Comment on the morphology of the red blood cells.
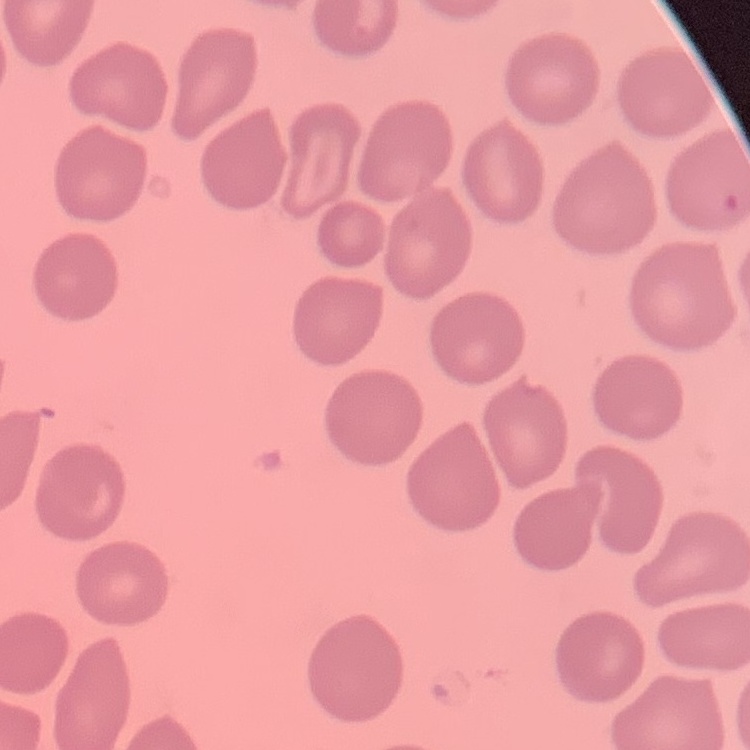
They show no rouleaux formation.

preparation = thin blood smear
image type = square crop of a larger photomicrograph
stain = Field's or Giemsa